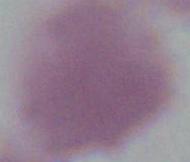

modality = micrograph
identification = erythrocyte
magnification = 1000x